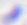
Summary:
  - Modality: photomicrograph
  - Magnification: 400x
  - Identification: Toxoplasma gondii